Report the malaria status of this cell.
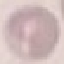

It is uninfected.

Acquired by smartphone through the microscope eyepiece. Thin smear of blood. Automatically extracted cell patch, resized to 64 × 64 pixels. Giemsa stain.